Classify this cell by malaria status.
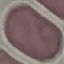

Uninfected.

capture = smartphone camera at the microscope eyepiece
image type = automatically extracted cell patch, resized to 64 × 64 pixels
preparation = thin smear
stain = Giemsa